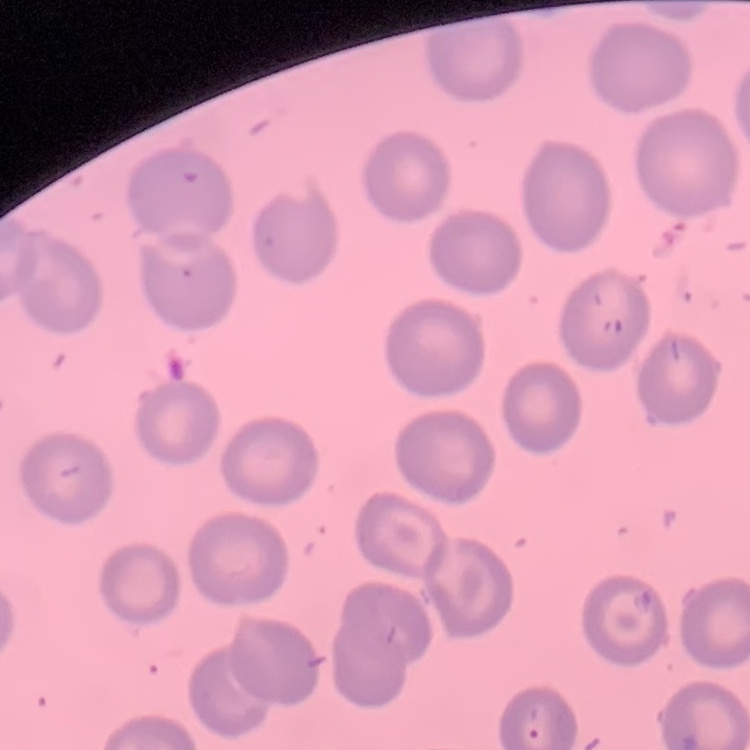
erythrocyte morphology = no rouleaux formation
stain = Field's or Giemsa
preparation = thin blood film
image type = one tile cut from a larger photomicrograph